Name the blood parasite species.
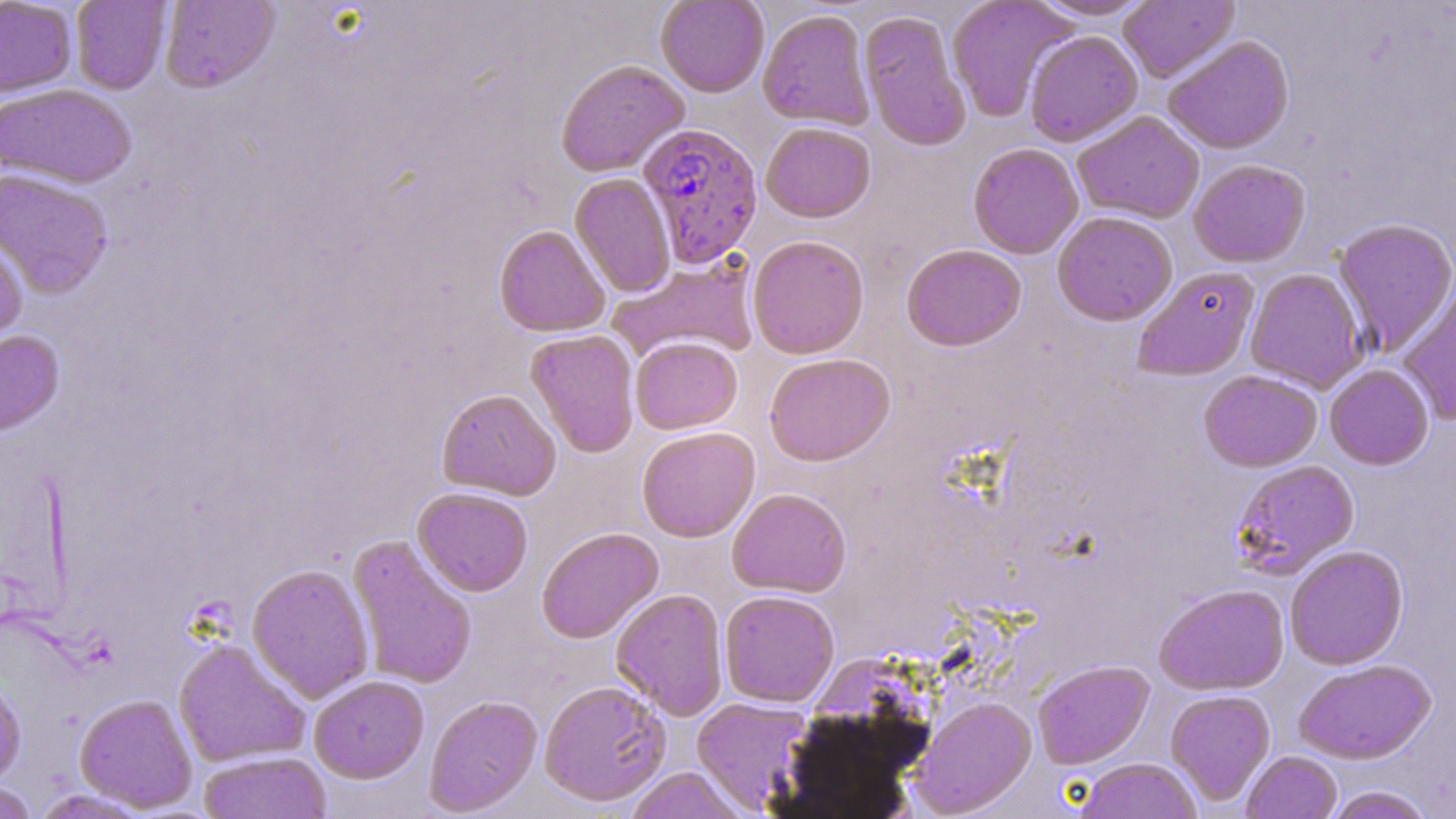

Plasmodium falciparum.

Approximate bounding boxes as (x1, y1, x2, y2) in pixels. Uninfected red blood cell locations: (0, 0, 77, 97), (71, 0, 171, 94), (159, 0, 280, 93), (656, 0, 769, 97), (946, 0, 1076, 122), (1030, 0, 1154, 20), (1118, 0, 1239, 83), (758, 9, 875, 129), (859, 10, 971, 151), (1024, 30, 1143, 147), (1162, 35, 1295, 154), (556, 59, 689, 177), (0, 84, 136, 189), (1072, 111, 1205, 224), (760, 121, 876, 222), (968, 142, 1084, 259), (1188, 159, 1311, 267), (0, 168, 113, 299), (570, 173, 676, 297), (1052, 211, 1178, 325), (1333, 218, 1456, 356), (494, 224, 610, 337), (0, 234, 28, 350), (747, 234, 870, 359), (901, 243, 1027, 350), (607, 256, 760, 365), (1132, 265, 1260, 381), (1245, 268, 1368, 393), (1397, 279, 1456, 427), (526, 329, 640, 458), (0, 330, 64, 435), (630, 337, 742, 434), (764, 353, 895, 466), (1324, 364, 1434, 470), (1198, 369, 1322, 472), (436, 388, 561, 500), (636, 426, 760, 542), (1230, 459, 1359, 579), (412, 487, 533, 596), (726, 488, 851, 597), (536, 527, 663, 644), (348, 534, 478, 690), (1284, 545, 1408, 670), (247, 563, 375, 703), (1153, 584, 1289, 695), (611, 588, 729, 720), (719, 590, 839, 707), (173, 638, 311, 768), (1293, 659, 1435, 764), (1033, 660, 1154, 769), (0, 672, 26, 788), (309, 675, 429, 783), (538, 680, 672, 806), (1165, 690, 1275, 806), (75, 693, 197, 812), (424, 694, 542, 816), (912, 696, 1037, 816), (691, 697, 814, 814), (198, 751, 333, 818), (1241, 751, 1342, 819), (1076, 758, 1203, 819), (624, 767, 748, 819), (0, 781, 39, 819), (1325, 786, 1435, 819), (30, 789, 152, 818). Plasmodium falciparum-infected red blood cell locations: (637, 121, 764, 267). Thin blood smear. Single field of view. Captured at 1000x magnification. Light microscopy. May-Grünwald-Giemsa-stained preparation. Image is 1456×819 pixels.